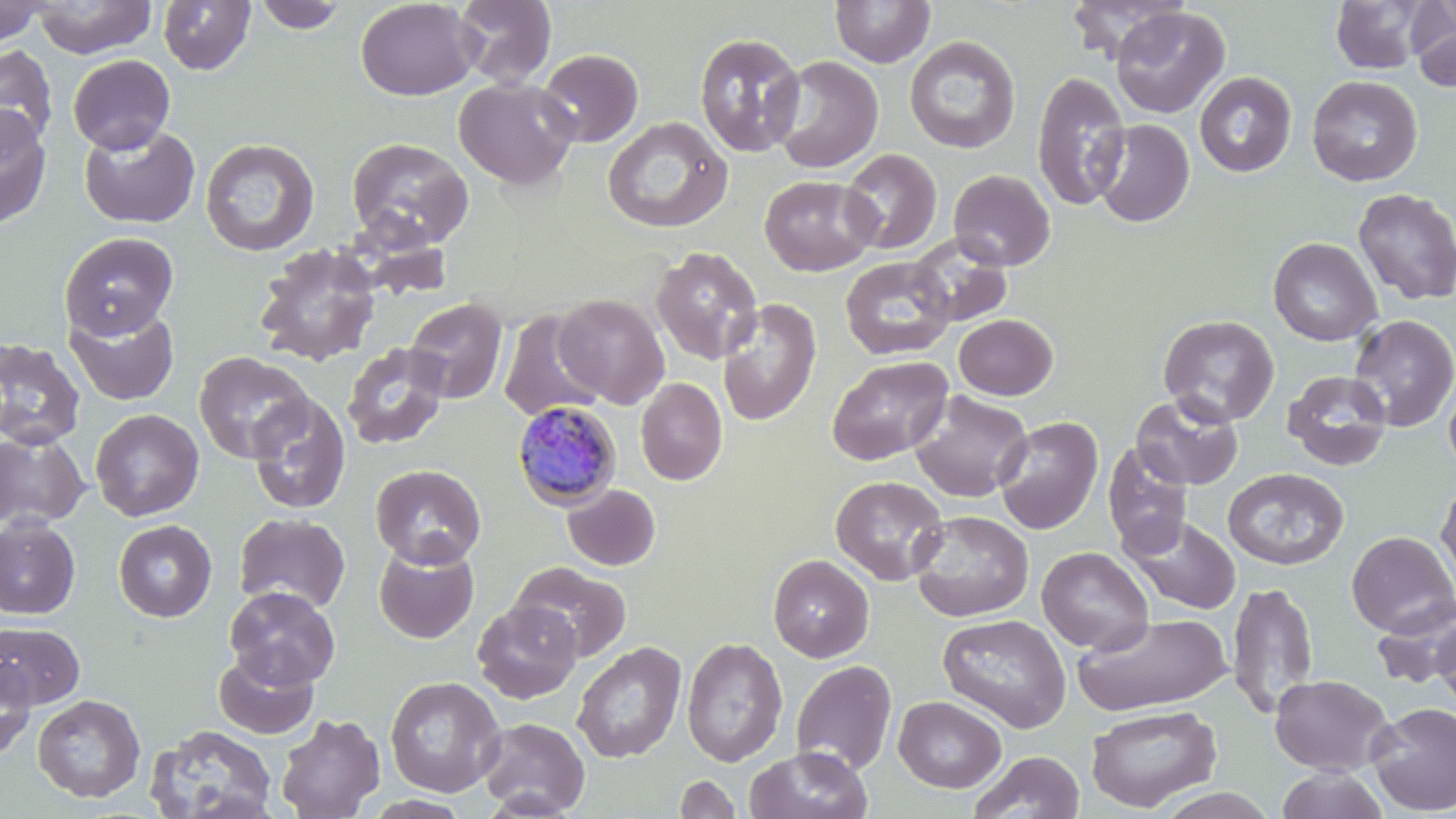

Summary:
  - Coordinate format: approximate bounding boxes as named x1/y1/x2/y2 corners in pixels
  - Uninfected red blood cell locations: (x1=32, y1=0, x2=157, y2=58), (x1=355, y1=0, x2=479, y2=100), (x1=453, y1=0, x2=556, y2=89), (x1=830, y1=0, x2=935, y2=67), (x1=1064, y1=0, x2=1189, y2=64), (x1=1330, y1=0, x2=1435, y2=74), (x1=0, y1=1, x2=51, y2=46), (x1=158, y1=1, x2=255, y2=75), (x1=253, y1=1, x2=348, y2=33), (x1=1408, y1=2, x2=1456, y2=91), (x1=1111, y1=6, x2=1229, y2=119), (x1=695, y1=31, x2=806, y2=157), (x1=904, y1=36, x2=1021, y2=153), (x1=0, y1=44, x2=58, y2=149), (x1=538, y1=48, x2=643, y2=147), (x1=68, y1=54, x2=175, y2=154), (x1=769, y1=55, x2=884, y2=174), (x1=1032, y1=69, x2=1130, y2=211), (x1=1194, y1=71, x2=1296, y2=177), (x1=1307, y1=75, x2=1423, y2=186), (x1=454, y1=78, x2=578, y2=190), (x1=0, y1=104, x2=52, y2=229), (x1=603, y1=116, x2=732, y2=233), (x1=1091, y1=118, x2=1195, y2=228), (x1=72, y1=123, x2=188, y2=340), (x1=79, y1=123, x2=201, y2=229), (x1=346, y1=136, x2=473, y2=248), (x1=200, y1=137, x2=320, y2=257), (x1=839, y1=148, x2=942, y2=254), (x1=948, y1=169, x2=1055, y2=271), (x1=759, y1=175, x2=879, y2=276), (x1=1352, y1=188, x2=1456, y2=305), (x1=59, y1=231, x2=179, y2=339), (x1=907, y1=235, x2=1012, y2=328), (x1=1267, y1=237, x2=1381, y2=346), (x1=254, y1=243, x2=382, y2=367), (x1=650, y1=246, x2=763, y2=364), (x1=840, y1=256, x2=955, y2=359), (x1=554, y1=294, x2=669, y2=408), (x1=405, y1=297, x2=508, y2=404), (x1=716, y1=298, x2=821, y2=426), (x1=64, y1=305, x2=180, y2=406), (x1=497, y1=309, x2=607, y2=423), (x1=1158, y1=313, x2=1279, y2=427), (x1=953, y1=314, x2=1058, y2=399), (x1=1348, y1=314, x2=1456, y2=433), (x1=0, y1=339, x2=86, y2=452), (x1=341, y1=342, x2=451, y2=451), (x1=194, y1=351, x2=314, y2=463), (x1=827, y1=356, x2=953, y2=465), (x1=1282, y1=369, x2=1392, y2=471), (x1=1443, y1=369, x2=1456, y2=480), (x1=635, y1=378, x2=727, y2=485), (x1=910, y1=391, x2=1033, y2=502), (x1=246, y1=392, x2=351, y2=514), (x1=1130, y1=392, x2=1244, y2=490), (x1=90, y1=409, x2=204, y2=520), (x1=993, y1=416, x2=1103, y2=535), (x1=0, y1=431, x2=91, y2=530), (x1=1102, y1=443, x2=1194, y2=559), (x1=371, y1=464, x2=486, y2=568), (x1=1222, y1=467, x2=1350, y2=569), (x1=831, y1=475, x2=948, y2=586), (x1=1435, y1=479, x2=1456, y2=596), (x1=562, y1=484, x2=660, y2=571), (x1=910, y1=511, x2=1034, y2=622), (x1=234, y1=512, x2=351, y2=613), (x1=1124, y1=516, x2=1241, y2=615), (x1=0, y1=517, x2=81, y2=620), (x1=113, y1=519, x2=217, y2=622), (x1=1346, y1=530, x2=1455, y2=637), (x1=374, y1=542, x2=479, y2=643), (x1=1036, y1=546, x2=1154, y2=653), (x1=779, y1=552, x2=885, y2=773), (x1=768, y1=554, x2=874, y2=662), (x1=511, y1=561, x2=632, y2=662), (x1=1227, y1=580, x2=1319, y2=720), (x1=224, y1=586, x2=341, y2=689), (x1=1371, y1=594, x2=1456, y2=690), (x1=472, y1=600, x2=582, y2=702), (x1=1071, y1=612, x2=1232, y2=716), (x1=936, y1=613, x2=1072, y2=733), (x1=1434, y1=620, x2=1456, y2=713), (x1=0, y1=622, x2=85, y2=709), (x1=681, y1=637, x2=788, y2=766), (x1=572, y1=641, x2=686, y2=762), (x1=213, y1=650, x2=321, y2=740), (x1=0, y1=655, x2=37, y2=759), (x1=790, y1=659, x2=897, y2=775), (x1=1270, y1=673, x2=1394, y2=775), (x1=385, y1=675, x2=505, y2=797), (x1=32, y1=694, x2=145, y2=802), (x1=893, y1=695, x2=1006, y2=793), (x1=1366, y1=701, x2=1456, y2=814), (x1=1086, y1=704, x2=1222, y2=812), (x1=275, y1=713, x2=385, y2=819), (x1=476, y1=716, x2=590, y2=817), (x1=145, y1=724, x2=278, y2=819), (x1=745, y1=745, x2=873, y2=819), (x1=970, y1=751, x2=1085, y2=818), (x1=1274, y1=767, x2=1391, y2=819), (x1=673, y1=774, x2=743, y2=818), (x1=1153, y1=788, x2=1280, y2=819)
  - Plasmodium malariae-infected red blood cell locations: (x1=511, y1=400, x2=623, y2=510)
  - Slide-level diagnosis: Plasmodium malariae
  - Modality: light microscopy
  - Preparation: thin blood film
  - Magnification: 1000x
  - Field of view: one of a larger specimen
  - Image size: 1456×819 pixels
  - Stain: May-Grünwald-Giemsa